Name the parasite shown.
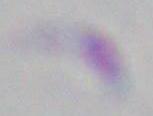

This is Toxoplasma gondii.

Summary:
  - Modality: photomicrograph
  - Magnification: 1000x